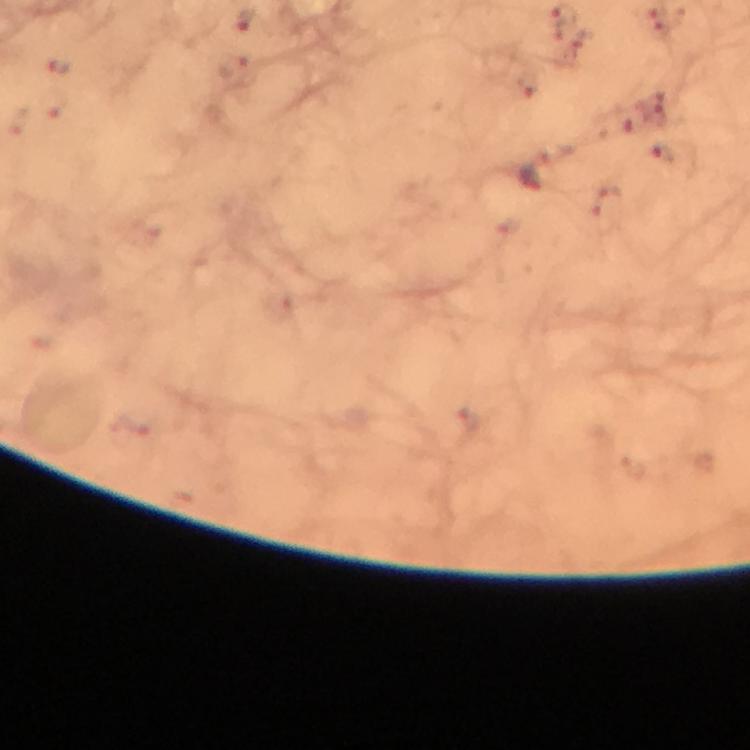

Approximate centers as (x, y) in pixels.
Summary:
  - Malaria parasite locations: (531, 178)
  - Stain: Giemsa
  - Image size: 750×750 pixels
  - Capture: smartphone mounted on the microscope
  - Immersion oil: used
  - Preparation: thick blood film
  - Magnification: 100x
  - Cropped from: one field of view
  - Context: from a diagnostic examination for malaria